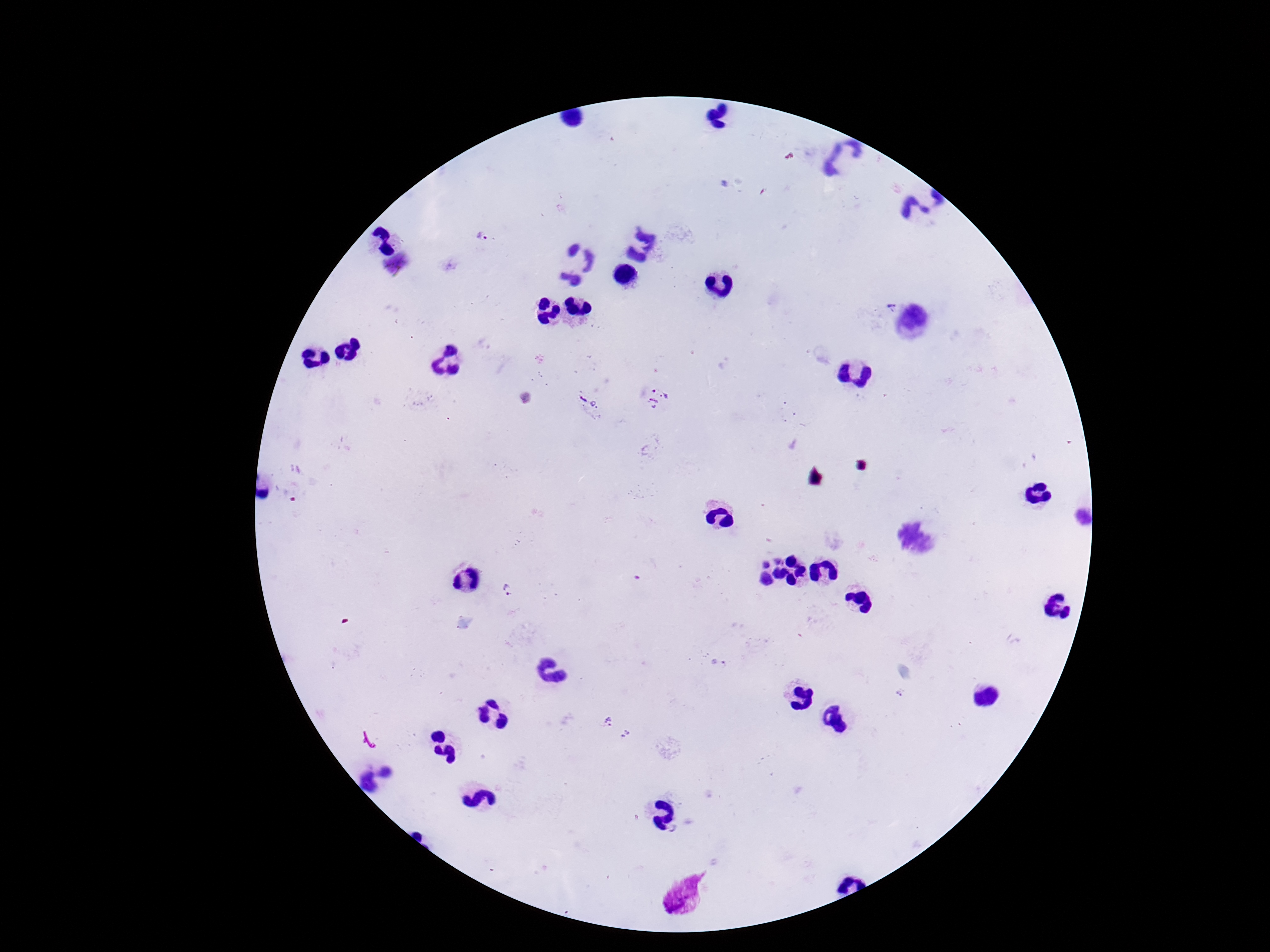
Approximate centers as [x, y] in pixels.
Summary:
  - Plasmodium parasite locations: [482, 235], [893, 307], [657, 398], [586, 401], [508, 589], [718, 664], [901, 693], [603, 719], [627, 735]
  - Field of view: one from this slide
  - Patient malaria status: infected
  - Image size: 1270×952 pixels
  - Magnification: 100x
  - Stain: Giemsa
  - Capture: smartphone camera through the microscope eyepiece
  - Preparation: thick blood film